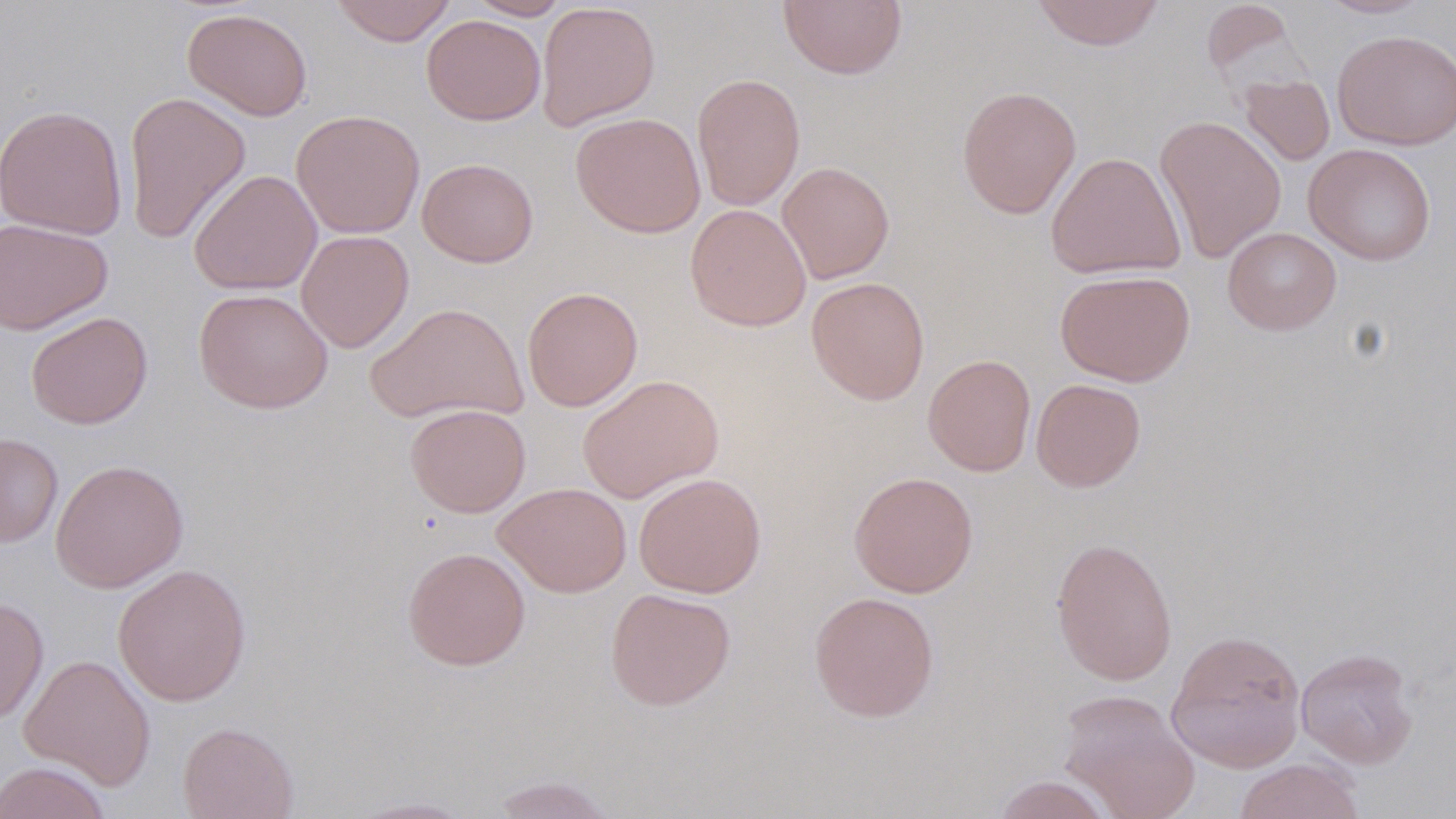

Summary:
  - Coordinate format: approximate bounding boxes as (x1, y1, x2, y2) in pixels
  - Uninfected red blood cell locations: (329, 0, 457, 46), (467, 0, 570, 20), (777, 0, 908, 80), (1029, 0, 1166, 51), (1315, 0, 1435, 20), (1199, 1, 1302, 88), (536, 2, 661, 131), (182, 7, 313, 121), (422, 14, 546, 126), (1332, 30, 1456, 150), (691, 73, 806, 211), (1238, 74, 1335, 166), (956, 85, 1082, 219), (122, 91, 252, 246), (0, 104, 128, 239), (291, 109, 425, 238), (570, 111, 706, 237), (1154, 114, 1287, 263), (1303, 143, 1436, 266), (1046, 151, 1185, 279), (417, 158, 539, 268), (776, 161, 895, 284), (188, 169, 322, 295), (685, 203, 812, 331), (0, 216, 113, 334), (1222, 227, 1341, 335), (296, 230, 414, 353), (1055, 269, 1195, 386), (806, 276, 930, 405), (522, 286, 643, 411), (194, 287, 333, 413), (365, 301, 529, 425), (26, 311, 153, 429), (922, 354, 1036, 476), (577, 374, 723, 503), (1031, 378, 1146, 492), (405, 403, 531, 517), (0, 432, 64, 548), (50, 459, 188, 592), (633, 472, 766, 598), (848, 472, 979, 597), (493, 482, 632, 598), (1050, 536, 1178, 686), (402, 546, 531, 671), (112, 563, 251, 706), (605, 587, 736, 710), (808, 591, 940, 723), (0, 595, 49, 725), (1166, 629, 1307, 772), (1295, 648, 1419, 769), (18, 654, 157, 791), (1056, 688, 1200, 819), (177, 721, 299, 819), (1233, 758, 1366, 819), (0, 761, 113, 819), (487, 774, 621, 818), (990, 774, 1117, 819), (345, 796, 480, 818)
  - Slide-level diagnosis: negative for blood parasites
  - Field of view: single
  - Preparation: thin blood film
  - Magnification: 1000x
  - Modality: optical microscopy
  - Stain: May-Grünwald-Giemsa
  - Image size: 1456×819 pixels